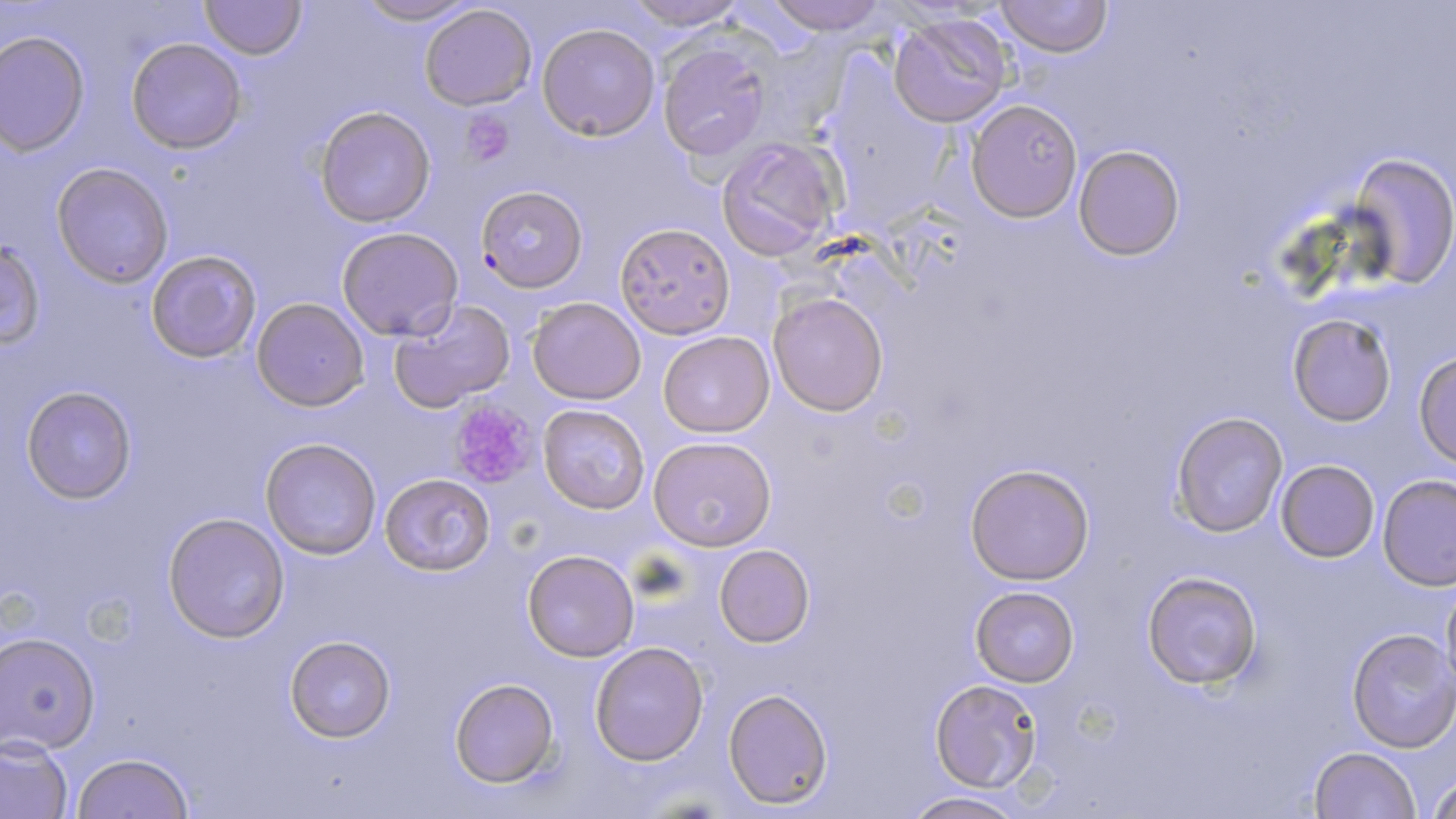

Approximate bounding boxes as (x1,y1)-(x2,y2) corner pairs in pixels. Uninfected red blood cell locations: (201,0)-(305,59), (351,0)-(480,25), (620,0)-(751,28), (761,0)-(893,34), (995,1)-(1111,57), (418,4)-(538,112), (887,12)-(1013,126), (536,22)-(660,140), (0,30)-(89,153), (127,37)-(246,153), (658,41)-(771,162), (966,98)-(1081,222), (313,104)-(437,228), (716,135)-(844,260), (1073,143)-(1185,261), (1347,154)-(1455,288), (51,162)-(173,289), (615,222)-(736,337), (336,226)-(463,340), (1,239)-(44,349), (145,249)-(263,364), (768,291)-(890,415), (528,296)-(646,404), (252,297)-(369,411), (388,297)-(515,414), (1287,313)-(1397,426), (659,331)-(773,437), (1412,352)-(1456,469), (21,386)-(137,505), (539,402)-(650,513), (1171,411)-(1287,537), (261,436)-(382,558), (648,436)-(777,552), (1275,460)-(1380,562), (964,461)-(1095,586), (380,472)-(497,578), (1377,473)-(1456,588), (162,513)-(290,642), (714,543)-(816,650), (521,549)-(639,662), (1141,570)-(1263,690), (1441,581)-(1456,702), (969,584)-(1081,688), (1347,629)-(1456,751), (0,632)-(100,755), (284,635)-(395,742), (589,641)-(709,765), (929,677)-(1047,793), (449,678)-(557,789), (723,687)-(832,808), (0,736)-(75,818), (1309,747)-(1420,819), (70,752)-(194,819), (1427,772)-(1456,817), (899,792)-(1028,819). Plasmodium falciparum-infected red blood cell locations: (474,188)-(587,295). Platelet locations: (458,108)-(515,168), (448,400)-(540,489). Slide-level diagnosis: Plasmodium falciparum. Thin blood smear. Optical microscopy. May-Grünwald-Giemsa stain. Image is 1456×819 pixels. One field of a larger specimen. 1000x magnification.